Give the position of every Plasmodium falciparum parasite, noting its life-cycle stage.
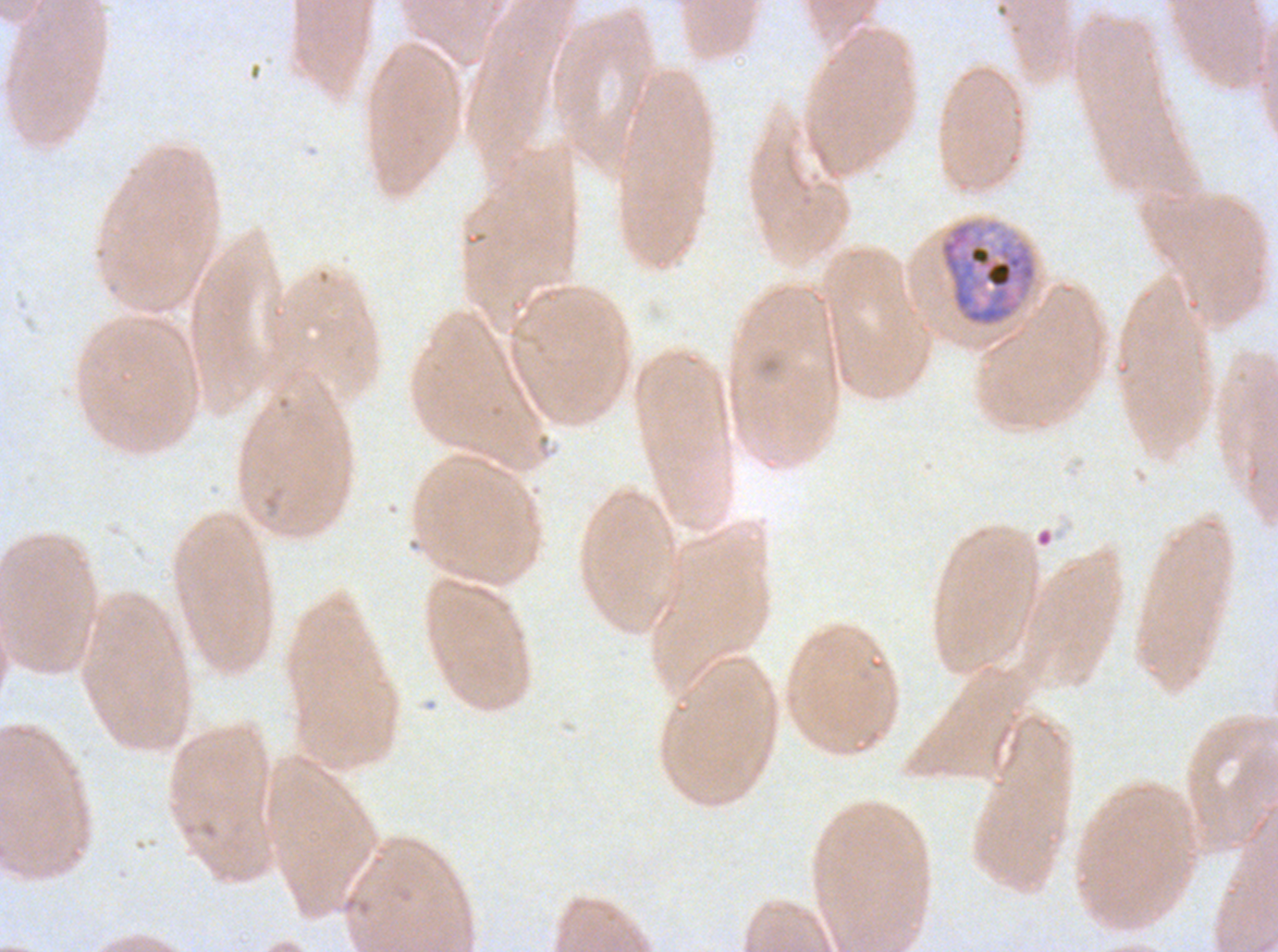

Approximate bounding boxes as [x1, y1, x2, y2] in pixels.
Early schizonts: [938, 218, 1038, 328].
No rings, late-ring/early-trophozoite forms, mid trophozoites, late trophozoites, late schizonts, segmenters, or gametocytes observed.

{
  "image_size": "1278×952 pixels",
  "stain": "Giemsa",
  "preparation": "thin blood smear",
  "field_of_view": "one sub-image of a larger composite",
  "specimen": "ex-vivo Plasmodium falciparum culture from a patient in The Gambia, grown for 24 to 48 hours"
}